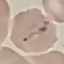
Malaria status: parasitized. Automatically extracted cell patch, resized to 64 × 64 pixels. Acquired by smartphone through the microscope eyepiece. Thin blood smear. Giemsa stain.